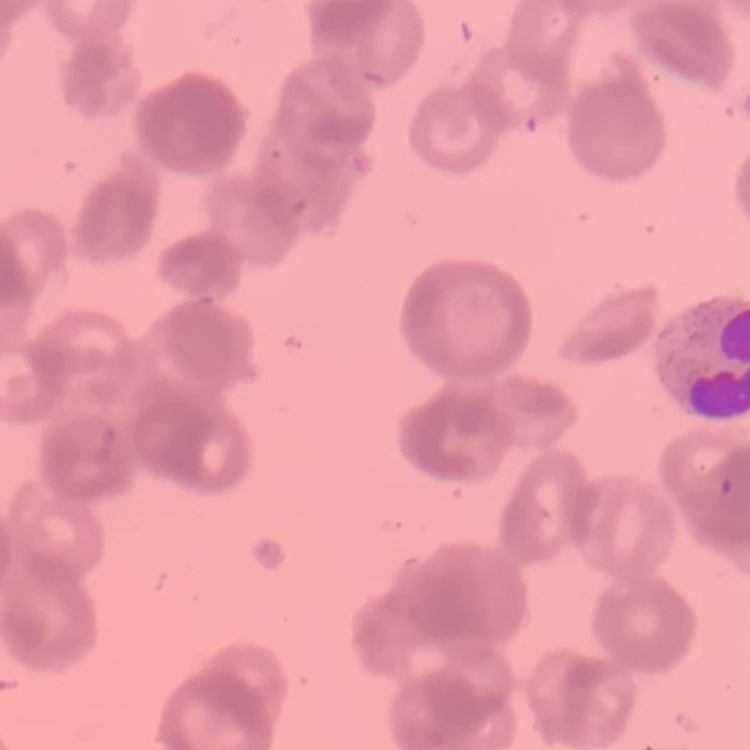
red blood cell morphology = rouleaux formation
preparation = thin peripheral smear
image type = square crop of a larger photomicrograph
stain = Field's or Giemsa